Assess this cell for malaria.
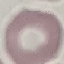
It is uninfected.

Thin smear of blood. Giemsa stain. Photographed with a smartphone camera at the microscope eyepiece. Automatically extracted cell patch, resized to 64 × 64 pixels.